Report the malaria status of this cell.
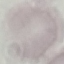

Uninfected.

Giemsa-stained preparation. Thin blood smear. Acquired by smartphone through the microscope eyepiece. Cell patch, automatically extracted from a larger field of view and resized to 64 × 64 pixels.